Assess the morphology of the red blood cells.
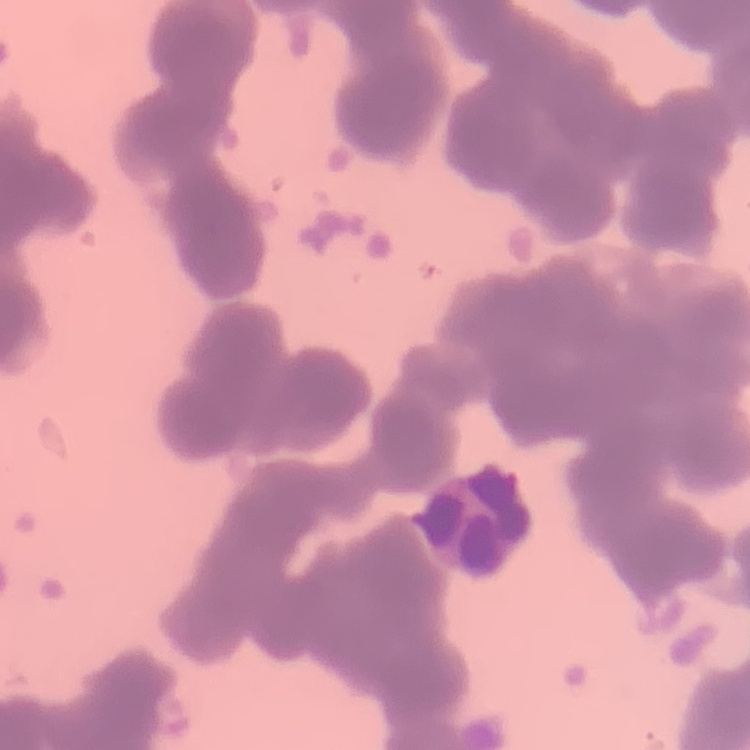

They show rouleaux formation.

Thin blood smear. Field's or Giemsa stain. Square crop of a larger photomicrograph.